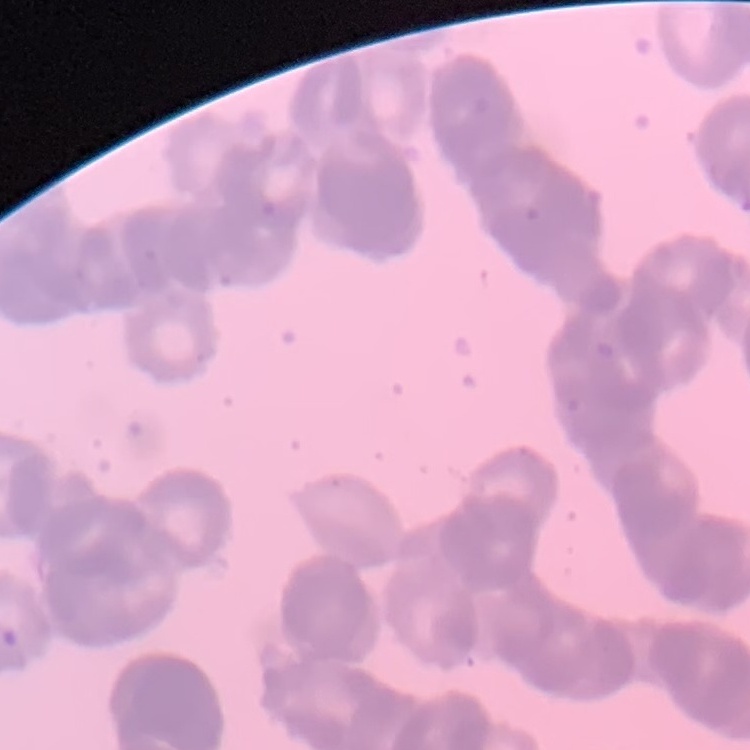
red_blood_cell_morphology: rouleaux formation
preparation: thin peripheral smear
stain: Field's or Giemsa
image_type: one tile cut from a larger photomicrograph